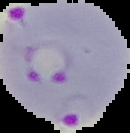
Summary:
  - Image type: segmented cell region with the area outside set to black
  - Image size: 130×133 pixels
  - Preparation: thin blood smear
  - Malaria status: parasitized